Report the malaria status of this cell.
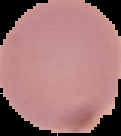
It is uninfected.

Summary:
  - Preparation: thin blood smear
  - Image size: 121×136 pixels
  - Image type: segmented cell region on a black background